State which parasite is depicted.
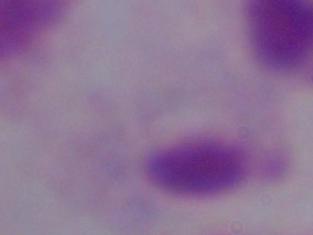

This is a trichomonad.

Captured at 1000x magnification. Micrograph.